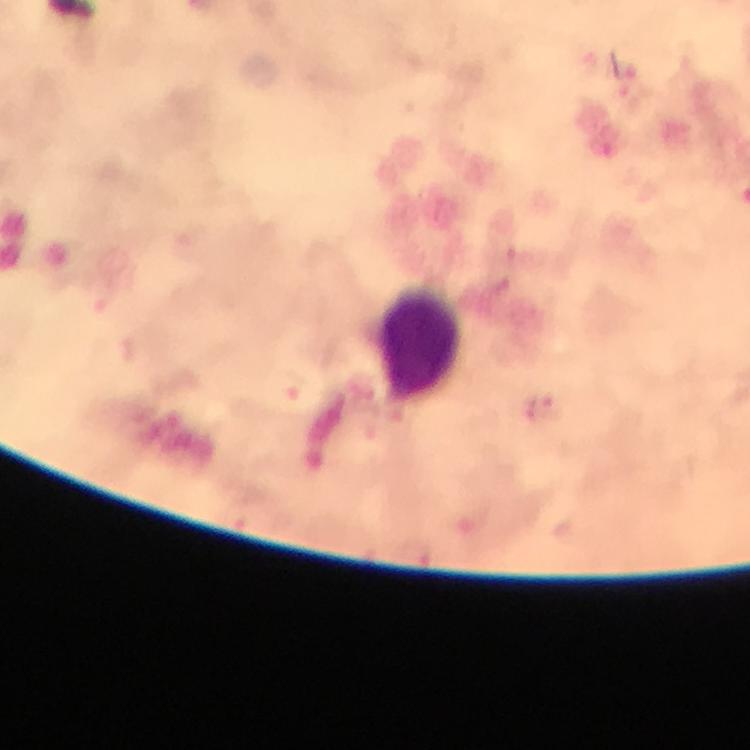

capture = smartphone photograph through a microscope
magnification = 100x
immersion oil = applied
leukocyte locations = approximate centers as (x, y) in pixels: (418, 342)
Plasmodium parasite locations = approximate centers as (x, y) in pixels: (546, 410)
preparation = thick blood smear
cropped from = one field of view
image size = 750×750 pixels
context = from a diagnostic examination for malaria
stain = Giemsa